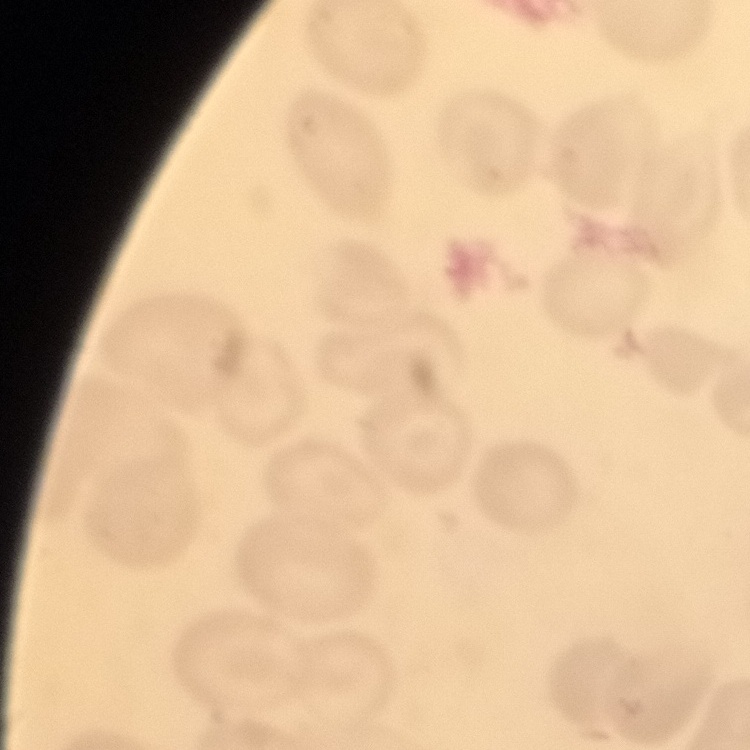

erythrocyte morphology = no rouleaux formation
image type = square crop of a larger photomicrograph
preparation = thin peripheral smear
stain = Field's or Giemsa